Identify the parasite.
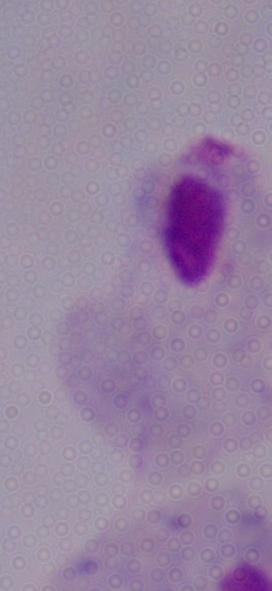
A trichomonad.

Summary:
  - Modality: photomicrograph
  - Magnification: 1000x